Locate every blood parasite and identify its species.
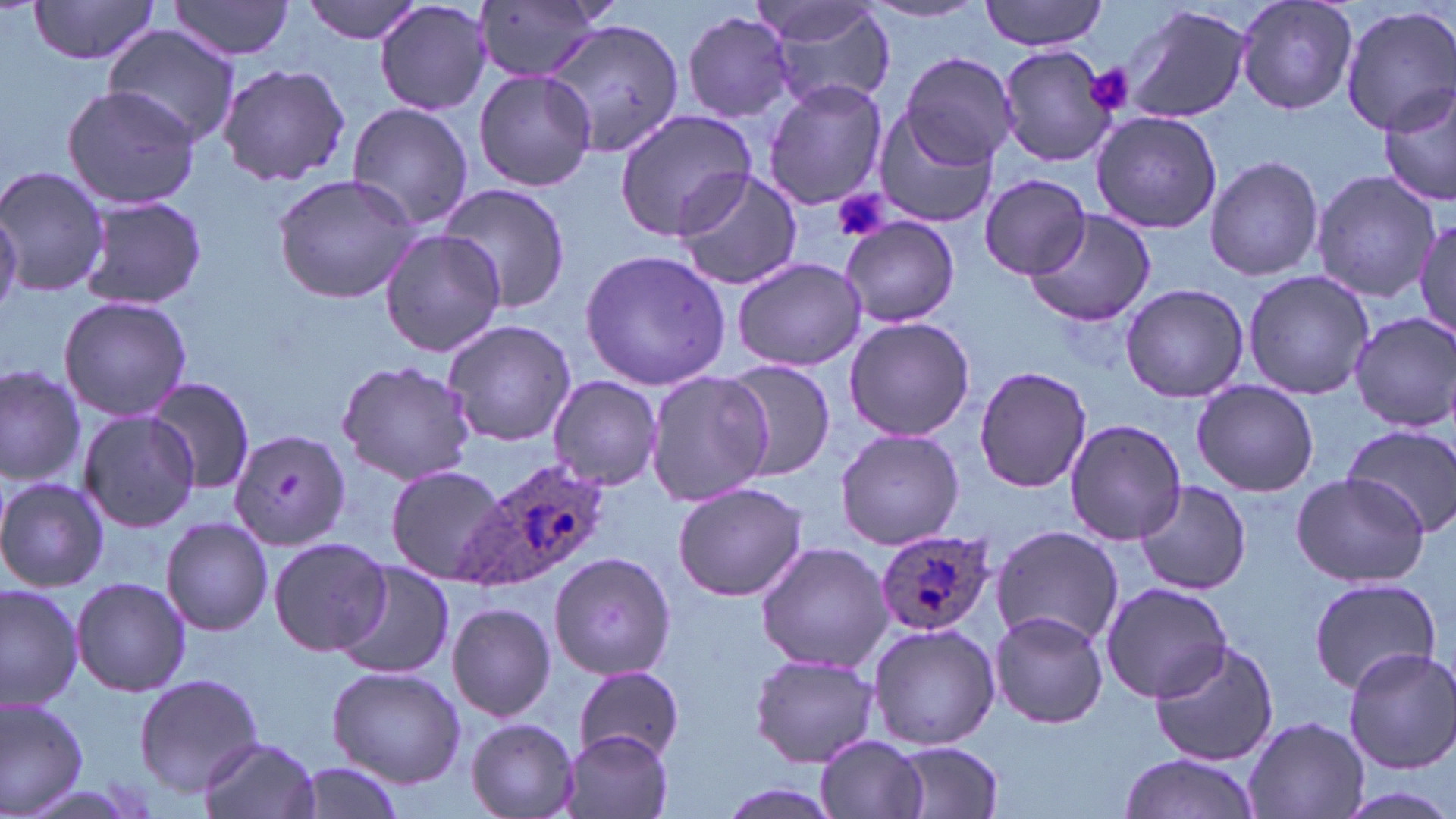

Approximate bounding boxes as (x1,y1)-(x2,y2) corner pairs in pixels.
Plasmodium ovale-infected red blood cells: (457,457)-(613,594), (872,527)-(996,637).
No Plasmodium falciparum, Plasmodium malariae, Plasmodium vivax, Babesia divergens, or Trypanosoma brucei observed.

Summary:
  - Platelet locations: (1083,63)-(1134,118), (831,189)-(890,243), (274,473)-(305,503)
  - Uninfected red blood cell locations: (26,0)-(163,66), (297,0)-(428,43), (981,0)-(1107,51), (1236,0)-(1358,116), (167,1)-(297,60), (374,1)-(492,116), (474,1)-(604,83), (759,2)-(896,109), (860,2)-(987,25), (1120,4)-(1251,124), (1341,4)-(1456,135), (681,10)-(798,123), (547,19)-(687,170), (104,28)-(240,145), (996,44)-(1120,168), (899,50)-(1017,168), (216,63)-(350,186), (472,67)-(598,193), (763,79)-(888,209), (61,84)-(203,208), (1380,84)-(1456,208), (345,102)-(476,232), (613,108)-(758,240), (1090,109)-(1221,235), (872,110)-(996,228), (1204,154)-(1324,282), (0,166)-(109,300), (672,169)-(804,291), (1311,170)-(1438,302), (272,172)-(421,305), (980,175)-(1092,278), (439,181)-(572,315), (78,194)-(206,312), (0,206)-(22,322), (1025,209)-(1156,326), (1411,213)-(1456,344), (838,216)-(963,329), (381,230)-(507,356), (579,247)-(733,391), (732,255)-(867,373), (1240,270)-(1373,398), (1119,283)-(1249,404), (58,296)-(191,423), (1348,310)-(1456,430), (842,316)-(975,443), (442,318)-(577,446), (335,357)-(479,486), (718,358)-(837,481), (0,363)-(88,491), (973,366)-(1093,493), (644,371)-(774,507), (547,375)-(663,490), (146,378)-(256,495), (1192,378)-(1319,497), (77,411)-(199,533), (1064,416)-(1185,545), (1341,424)-(1456,537), (835,428)-(964,550), (231,429)-(350,551), (385,464)-(510,584), (1288,471)-(1431,589), (0,477)-(110,593), (1134,480)-(1252,596), (673,482)-(807,602), (161,517)-(273,638), (991,525)-(1124,648), (268,535)-(394,657), (756,541)-(890,672), (549,551)-(677,680), (331,560)-(452,680), (1308,574)-(1443,695), (70,577)-(190,698), (0,582)-(84,712), (1101,583)-(1234,702), (446,602)-(555,721), (989,609)-(1108,729), (866,622)-(999,752), (1149,638)-(1278,766), (1340,646)-(1453,773), (749,652)-(881,768), (325,664)-(466,786), (574,665)-(686,763), (135,673)-(262,793), (0,696)-(88,816), (1244,717)-(1368,818), (464,718)-(580,819), (561,730)-(673,819), (815,734)-(930,819), (197,736)-(320,819), (888,741)-(1005,818), (1116,753)-(1261,819), (286,763)-(409,818), (709,781)-(849,819), (1332,788)-(1454,819)
  - Slide-level diagnosis: Plasmodium ovale
  - Field of view: one of a larger specimen
  - Image size: 1456×819 pixels
  - Magnification: 1000x
  - Stain: May-Grünwald-Giemsa
  - Preparation: thin blood smear
  - Modality: optical microscopy